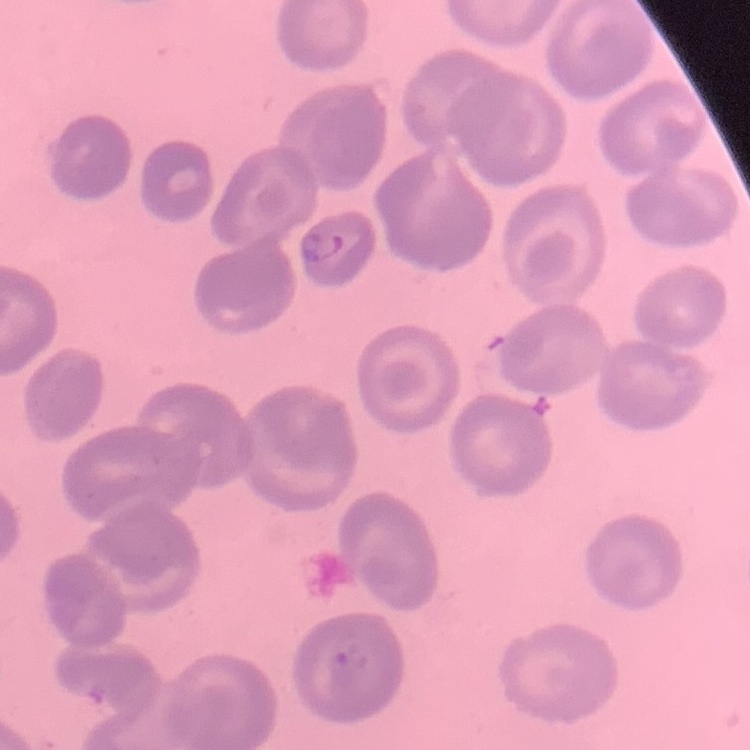

Summary:
  - Red blood cell morphology: no rouleaux formation
  - Image type: square crop of a larger photomicrograph
  - Preparation: thin blood film
  - Stain: Field's or Giemsa